Outline each blood parasite and name the species.
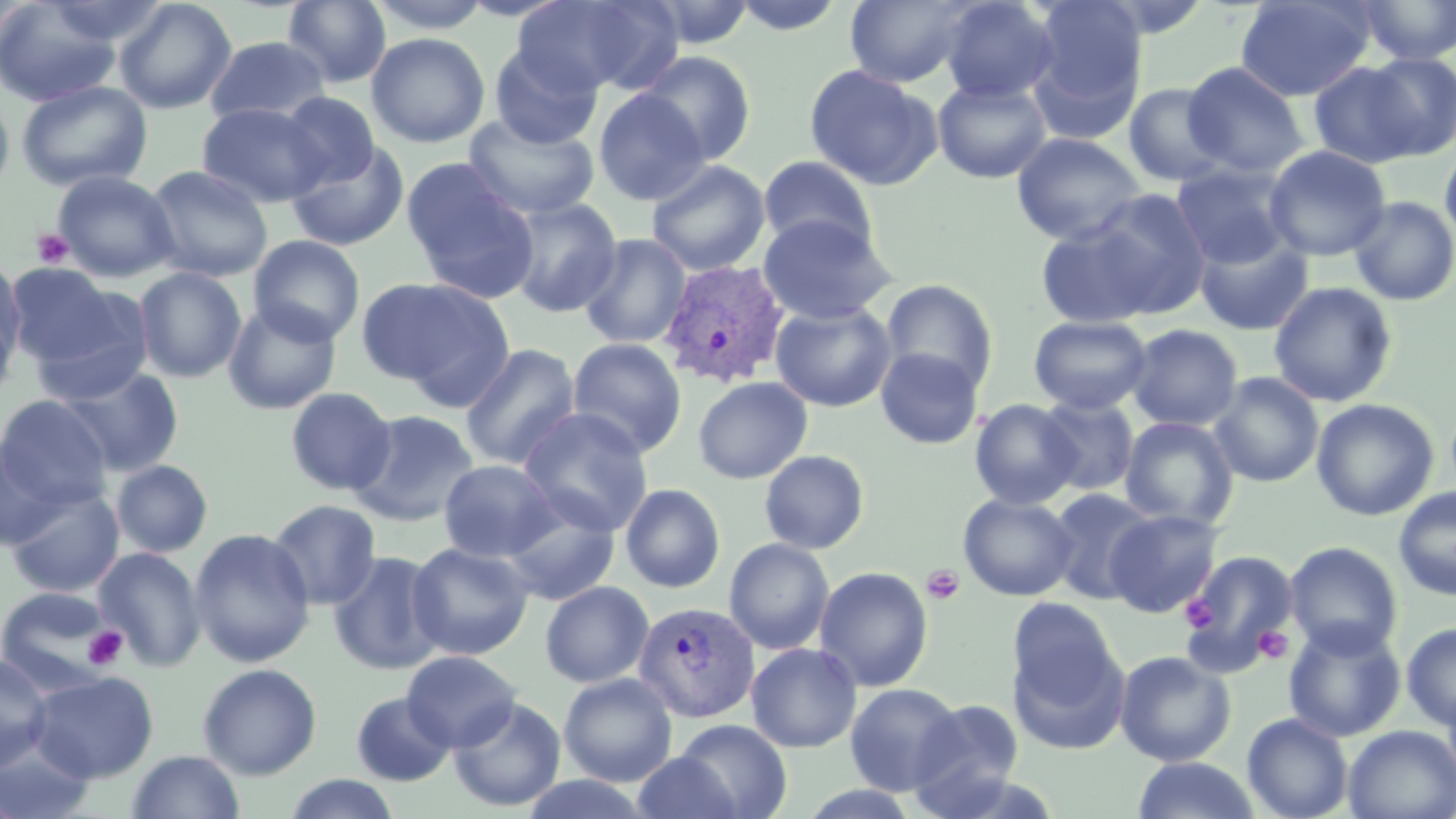
Approximate bounding boxes as [x1, y1, x2, y2] in pixels.
Plasmodium vivax-infected red blood cells: [658, 258, 790, 389], [633, 601, 759, 723].
No Plasmodium falciparum, Plasmodium ovale, Plasmodium malariae, Babesia divergens, or Trypanosoma brucei observed.

Summary:
  - Platelet locations: [33, 228, 74, 268], [921, 565, 965, 605], [1179, 596, 1217, 631], [1253, 624, 1294, 666], [84, 626, 129, 671]
  - Uninfected red blood cell locations: [114, 0, 237, 115], [282, 0, 392, 88], [366, 0, 494, 34], [513, 0, 680, 98], [728, 0, 850, 36], [844, 0, 978, 87], [938, 0, 1059, 104], [1025, 0, 1149, 135], [1235, 0, 1375, 101], [1355, 0, 1455, 65], [0, 1, 122, 106], [639, 1, 759, 49], [366, 32, 490, 148], [205, 35, 329, 125], [489, 44, 602, 149], [633, 51, 757, 165], [1359, 52, 1456, 161], [1309, 59, 1424, 168], [1182, 61, 1309, 177], [804, 64, 941, 191], [932, 78, 1053, 184], [16, 79, 152, 192], [1123, 82, 1231, 187], [593, 88, 710, 205], [279, 91, 380, 188], [0, 92, 14, 199], [196, 102, 329, 207], [463, 113, 599, 221], [1010, 131, 1147, 246], [285, 140, 410, 251], [1440, 141, 1456, 250], [1264, 145, 1391, 261], [757, 155, 879, 257], [403, 159, 540, 303], [646, 159, 770, 276], [1170, 161, 1298, 270], [145, 165, 273, 281], [52, 170, 179, 282], [1082, 188, 1212, 316], [1349, 196, 1456, 306], [503, 197, 623, 317], [757, 214, 896, 324], [1034, 219, 1164, 327], [1194, 231, 1313, 335], [578, 233, 692, 349], [248, 235, 365, 345], [0, 257, 24, 377], [4, 263, 125, 367], [133, 267, 247, 382], [359, 276, 509, 398], [880, 278, 999, 394], [1268, 281, 1397, 408], [25, 289, 154, 406], [223, 300, 341, 415], [770, 300, 897, 412], [0, 307, 18, 409], [1028, 315, 1152, 415], [1126, 324, 1243, 431], [567, 337, 687, 457], [459, 343, 581, 469], [875, 346, 984, 449], [60, 366, 183, 476], [1209, 372, 1324, 487], [693, 376, 812, 484], [285, 387, 396, 495], [1036, 395, 1139, 497], [1, 396, 112, 510], [969, 399, 1082, 509], [1311, 399, 1438, 521], [518, 407, 654, 536], [350, 409, 480, 526], [1120, 416, 1239, 530], [0, 439, 62, 549], [759, 450, 870, 554], [438, 459, 562, 562], [111, 460, 213, 558], [620, 483, 726, 592], [5, 486, 125, 597], [1393, 486, 1456, 600], [1047, 489, 1158, 604], [958, 493, 1078, 601], [498, 498, 620, 607], [268, 499, 381, 609], [1104, 509, 1223, 618], [189, 528, 315, 667], [724, 538, 835, 655], [407, 541, 535, 660], [1284, 541, 1403, 658], [93, 548, 207, 671], [1180, 550, 1299, 674], [329, 551, 447, 675], [814, 566, 934, 692], [540, 581, 654, 688], [0, 586, 118, 691], [1007, 611, 1125, 750], [1283, 619, 1406, 742], [1401, 622, 1456, 730], [746, 642, 862, 752], [401, 650, 522, 751], [1114, 650, 1237, 766], [0, 653, 52, 772], [197, 663, 322, 779], [28, 671, 158, 782], [558, 673, 678, 786], [1441, 677, 1456, 795], [844, 682, 963, 795], [351, 692, 456, 786], [448, 696, 566, 811], [909, 698, 1025, 813], [1242, 713, 1353, 818], [672, 719, 792, 819], [1343, 725, 1456, 819], [0, 737, 96, 819], [125, 750, 246, 819], [631, 751, 742, 819], [1131, 757, 1262, 818], [281, 774, 403, 818], [517, 775, 653, 818], [794, 785, 925, 819]
  - Slide-level diagnosis: Plasmodium vivax
  - Magnification: 1000x
  - Field of view: one of a larger specimen
  - Stain: May-Grünwald-Giemsa
  - Image size: 1456×819 pixels
  - Modality: optical microscopy
  - Preparation: thin blood smear